Assess this cell for malaria.
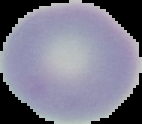
It is uninfected.

image size = 142×124 pixels
preparation = thin blood film
image type = cell region segmented out of the field of view; surrounding area masked to black